Identify the preparation type.
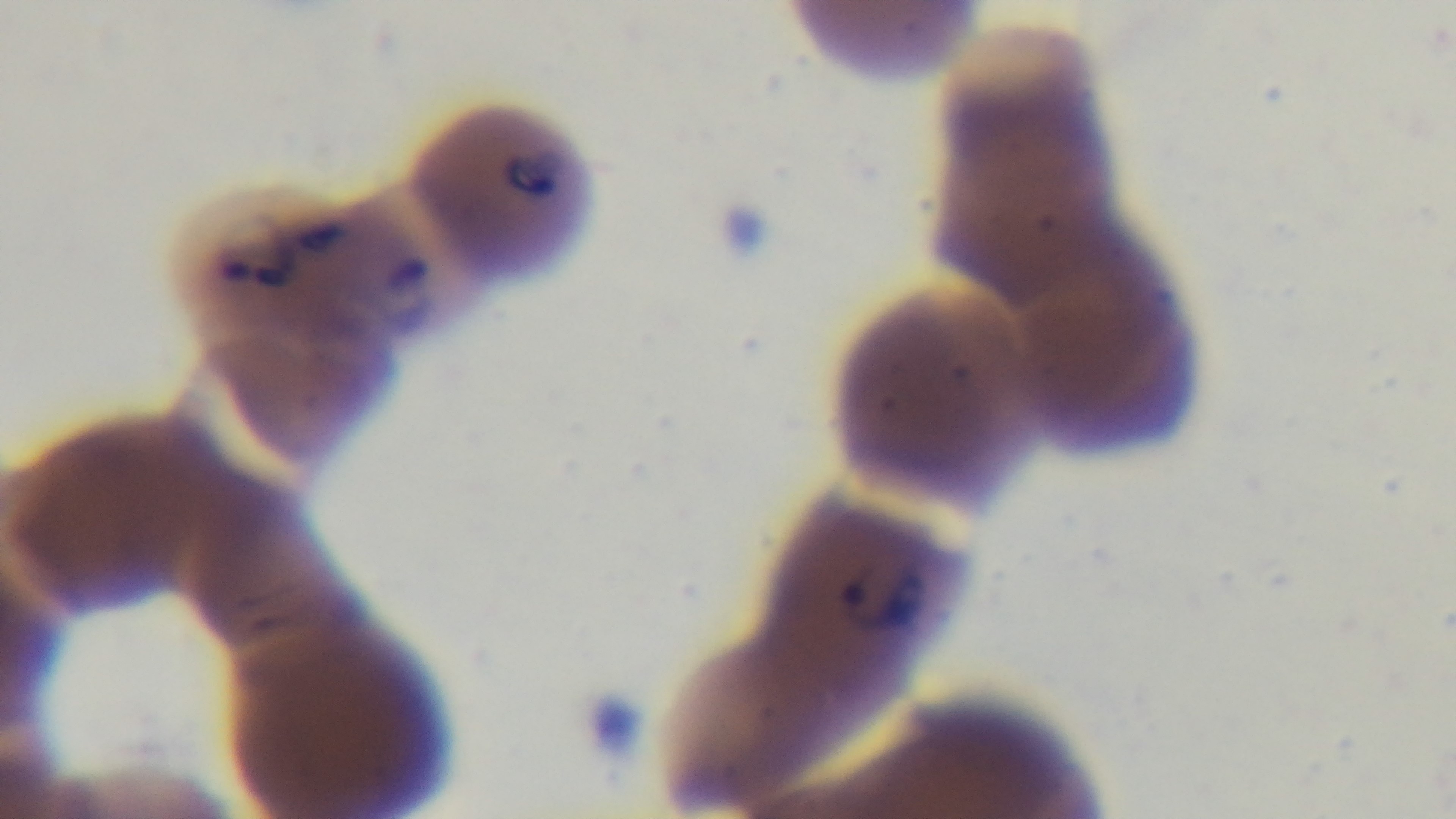
Thin.

{
  "modality": "light microscopy",
  "stain": "Giemsa",
  "malaria_status": "positive",
  "capture": "mounted 4K digital camera",
  "field_of_view": "single",
  "objective": "100x oil immersion"
}